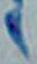

Summary:
  - Magnification: 1000x
  - Modality: micrograph
  - Identification: Toxoplasma gondii